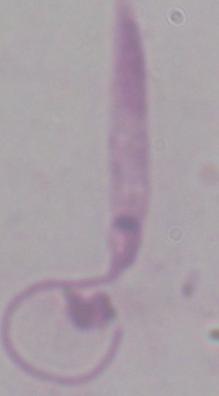
Summary:
  - Magnification: 1000x
  - Modality: micrograph
  - Identification: Leishmania